Outline each uninfected red blood cell.
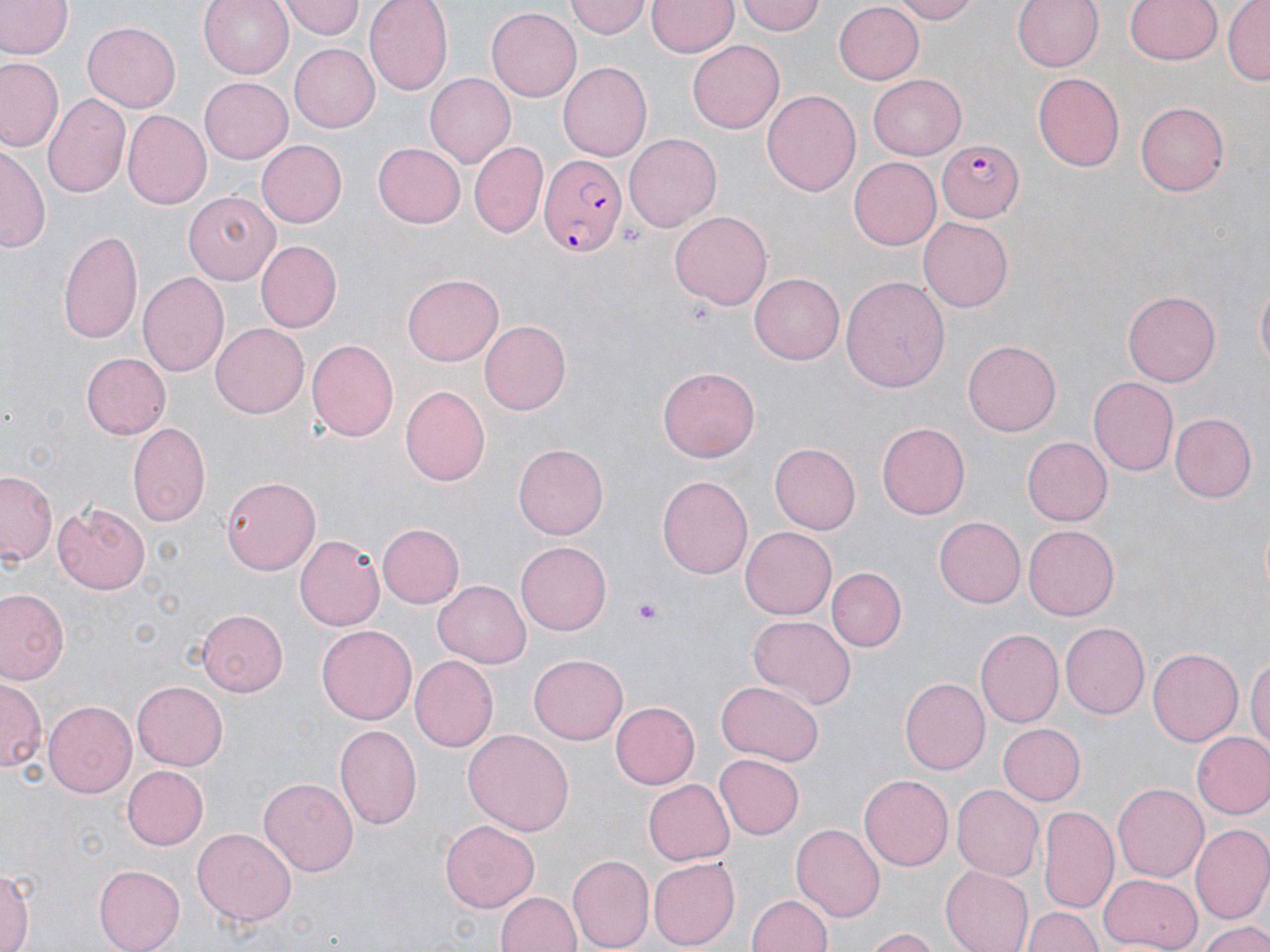

Approximate bounding boxes as (x1, y1, x2, y2) in pixels.
Uninfected red blood cells: (198, 0, 293, 78), (363, 0, 452, 95), (565, 0, 651, 39), (738, 0, 827, 36), (888, 0, 978, 23), (1011, 0, 1103, 74), (1121, 0, 1222, 68), (1224, 0, 1269, 86), (0, 1, 69, 59), (280, 1, 364, 40), (646, 1, 738, 59), (832, 2, 925, 84), (485, 8, 581, 103), (83, 21, 182, 111), (290, 42, 381, 133), (689, 42, 783, 133), (1, 57, 61, 152), (559, 62, 653, 160), (1032, 73, 1126, 170), (424, 74, 516, 168), (865, 75, 966, 159), (198, 76, 292, 163), (762, 89, 862, 196), (44, 93, 129, 199), (1136, 101, 1229, 197), (121, 109, 211, 208), (625, 133, 721, 231), (257, 139, 347, 228), (372, 142, 466, 228), (469, 142, 548, 237), (1, 143, 47, 254), (848, 156, 942, 250), (182, 191, 279, 284), (671, 212, 772, 310), (917, 217, 1012, 312), (58, 228, 142, 344), (256, 240, 342, 332), (136, 271, 230, 379), (403, 273, 504, 365), (749, 273, 845, 366), (840, 275, 950, 390), (1254, 280, 1269, 379), (1123, 289, 1222, 386), (480, 320, 572, 414), (211, 322, 309, 418), (307, 337, 400, 445), (963, 340, 1062, 435), (82, 353, 170, 438), (658, 364, 760, 462), (1088, 376, 1179, 476), (402, 385, 493, 486), (1168, 412, 1256, 502), (877, 422, 969, 520), (127, 423, 210, 526), (1023, 438, 1112, 524), (513, 443, 608, 539), (770, 443, 860, 535), (0, 470, 56, 566), (219, 475, 320, 574), (657, 475, 754, 580), (53, 500, 153, 594), (933, 516, 1025, 607), (376, 523, 464, 608), (1023, 523, 1119, 617), (740, 525, 835, 617), (295, 533, 385, 632), (516, 540, 610, 633), (828, 568, 905, 650), (433, 580, 531, 667), (1, 590, 68, 684), (197, 610, 289, 697), (747, 614, 855, 710), (1060, 621, 1149, 720), (318, 623, 419, 724), (977, 628, 1063, 728), (1148, 648, 1244, 747), (530, 653, 629, 744), (1247, 655, 1270, 757), (409, 656, 498, 753), (899, 677, 989, 776), (0, 680, 42, 775), (716, 681, 825, 766), (133, 682, 227, 771), (44, 700, 136, 799), (611, 701, 700, 790), (996, 723, 1084, 806), (336, 724, 422, 828), (462, 728, 572, 836), (1191, 731, 1270, 820), (715, 754, 804, 838), (122, 764, 207, 849), (859, 773, 954, 870), (259, 778, 359, 876), (643, 779, 734, 867), (1112, 782, 1207, 882), (953, 784, 1044, 880), (1038, 805, 1117, 912), (439, 819, 537, 912), (790, 823, 884, 920), (1192, 823, 1270, 922), (193, 827, 296, 925), (567, 853, 654, 952), (646, 857, 738, 950), (0, 864, 35, 952), (93, 864, 185, 951), (940, 866, 1033, 952), (1099, 873, 1201, 950), (496, 890, 582, 952), (746, 891, 834, 952), (1023, 906, 1103, 952), (1197, 920, 1268, 952), (863, 928, 939, 952).

Summary:
  - Platelet locations: (629, 597, 666, 623)
  - Plasmodium falciparum-infected red blood cell locations: (937, 137, 1023, 222), (537, 149, 625, 258)
  - Slide-level diagnosis: Plasmodium falciparum
  - Image size: 1270×952 pixels
  - Stain: May-Grünwald-Giemsa
  - Preparation: thin blood smear
  - Magnification: 1000x
  - Field of view: single
  - Modality: optical microscopy